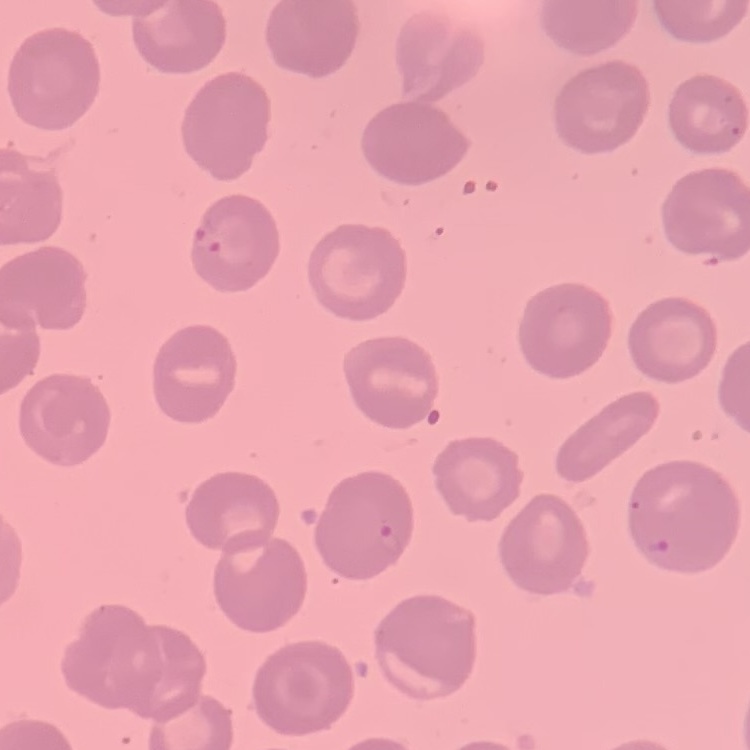 The red blood cells show no rouleaux formation. Field's or Giemsa stain. Thin peripheral smear. One tile cut from a larger photomicrograph.